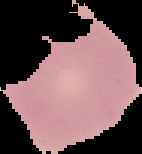
Malaria status: uninfected. Segmented cell region on a black background. From a thin blood smear. Image is 142×154 pixels.